Identify the parasite.
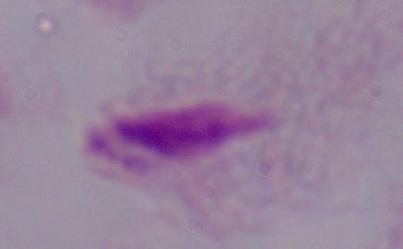
A trichomonad.

Photomicrograph. Captured at 1000x magnification.